Assess this cell for malaria.
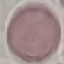

Uninfected.

Giemsa stain. Acquired by smartphone through the microscope eyepiece. Thin blood smear. Automatically extracted cell patch, resized to 64 × 64 pixels.